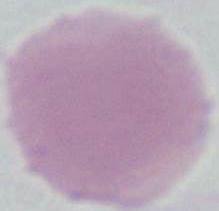
An erythrocyte is shown. Photomicrograph. 1000x magnification.